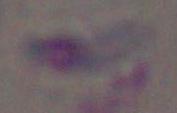

Summary:
  - Modality: micrograph
  - Identification: Toxoplasma gondii
  - Magnification: 1000x